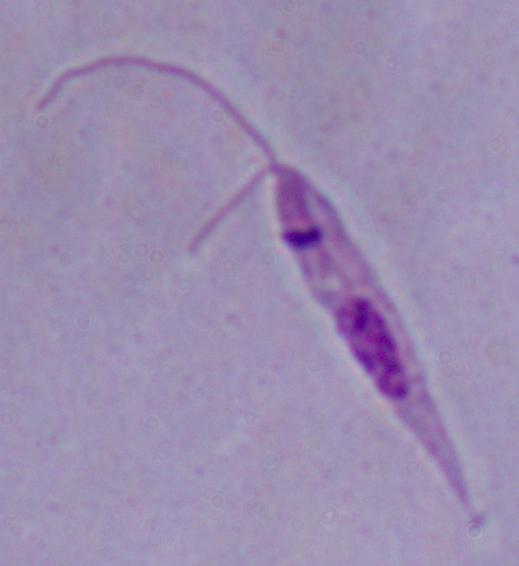

Summary:
  - Modality: photomicrograph
  - Identification: Leishmania
  - Magnification: 1000x